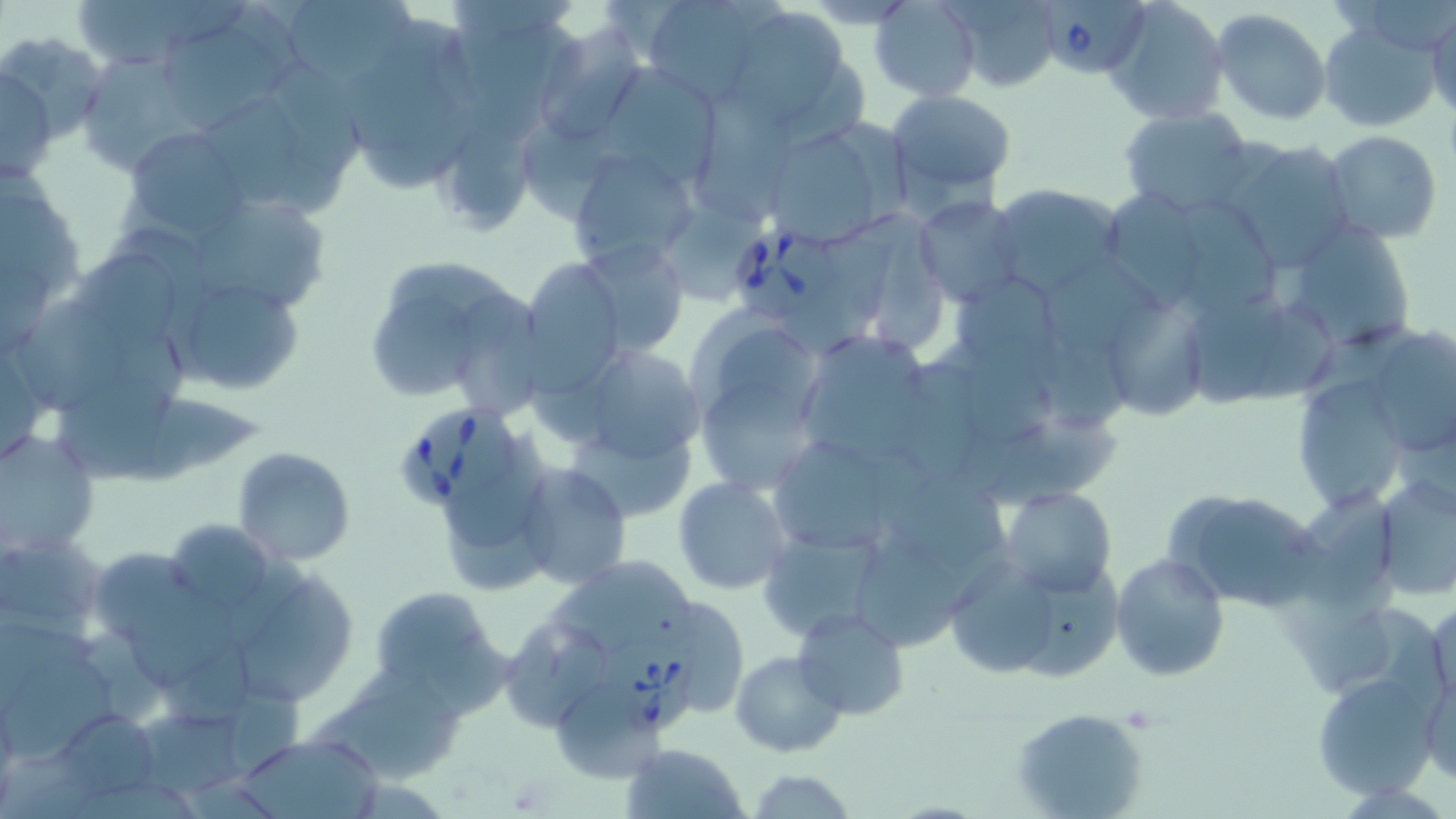
babesia_divergens_infected_red_blood_cell_locations: 'approximate bounding boxes as [x1, y1, x2, y2] in pixels: [1041, 0, 1149, 79], [724, 222, 840, 315], [399, 400, 516, 510], [599, 626, 695, 734]'
slide_level_diagnosis: Babesia divergens
modality: light microscopy
uninfected_red_blood_cell_locations: 'approximate bounding boxes as [x1, y1, x2, y2] in pixels: [72, 0, 208, 73], [640, 0, 775, 103], [933, 0, 1059, 91], [1105, 0, 1230, 126], [278, 1, 418, 95], [869, 1, 981, 100], [721, 4, 863, 136], [1211, 10, 1331, 125], [1428, 10, 1456, 118], [157, 19, 281, 130], [336, 19, 487, 192], [1318, 22, 1441, 131], [535, 27, 646, 149], [2, 34, 108, 146], [76, 52, 205, 176], [592, 60, 723, 188], [1, 64, 55, 185], [888, 90, 1019, 198], [204, 99, 304, 206], [1119, 106, 1256, 219], [430, 110, 545, 237], [757, 121, 901, 247], [122, 126, 252, 244], [1322, 130, 1443, 243], [1217, 139, 1358, 270], [566, 147, 698, 273], [987, 183, 1124, 297], [0, 188, 80, 303], [914, 195, 1026, 307], [196, 196, 330, 315], [873, 218, 949, 355], [1284, 219, 1419, 353], [574, 238, 690, 358], [68, 252, 179, 351], [516, 257, 628, 393], [1046, 257, 1162, 353], [958, 272, 1059, 360], [786, 276, 880, 353], [186, 285, 303, 397], [1097, 289, 1207, 426], [9, 295, 138, 410], [374, 295, 477, 399], [1191, 295, 1282, 404], [1257, 303, 1338, 403], [716, 327, 815, 406], [1363, 328, 1454, 457], [794, 329, 941, 470], [564, 341, 708, 471], [967, 345, 1076, 445], [1049, 347, 1136, 436], [903, 358, 991, 473], [58, 377, 174, 475], [1291, 377, 1413, 515], [702, 379, 809, 491], [133, 396, 262, 489], [984, 416, 1125, 511], [0, 429, 99, 554], [565, 431, 696, 518], [766, 432, 909, 557], [440, 433, 546, 545], [232, 447, 356, 566], [516, 465, 632, 590], [899, 471, 1005, 574], [672, 475, 793, 595], [1373, 476, 1456, 602], [1303, 486, 1400, 609], [999, 487, 1117, 599], [1164, 488, 1326, 611], [449, 506, 556, 594], [169, 518, 269, 610], [760, 529, 885, 638], [0, 535, 107, 640], [853, 541, 959, 654], [95, 546, 205, 644], [1112, 553, 1229, 682], [550, 558, 698, 649], [948, 558, 1059, 677], [1020, 561, 1125, 680], [242, 570, 356, 702], [124, 583, 237, 689], [369, 585, 507, 708], [677, 596, 754, 714], [1429, 600, 1455, 712], [1325, 605, 1451, 699], [792, 606, 910, 719], [510, 625, 608, 732], [161, 642, 263, 729], [730, 650, 845, 757], [7, 651, 112, 761], [1419, 659, 1455, 788], [1312, 671, 1439, 802], [550, 678, 666, 783], [324, 679, 464, 783], [230, 691, 304, 775], [1011, 707, 1151, 819], [49, 708, 163, 808], [149, 710, 247, 794], [235, 733, 382, 818], [620, 742, 749, 819], [746, 766, 857, 819]'
stain: May-Grünwald-Giemsa
preparation: thin blood film
image_size: 1456×819 pixels
field_of_view: one of a larger specimen
magnification: 1000x